Classify this cell by malaria status.
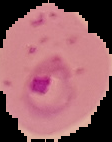

It is parasitized.

Summary:
  - Image type: segmented cell region with the area outside set to black
  - Image size: 112×142 pixels
  - Preparation: thin blood film